Locate every blood parasite and identify its species.
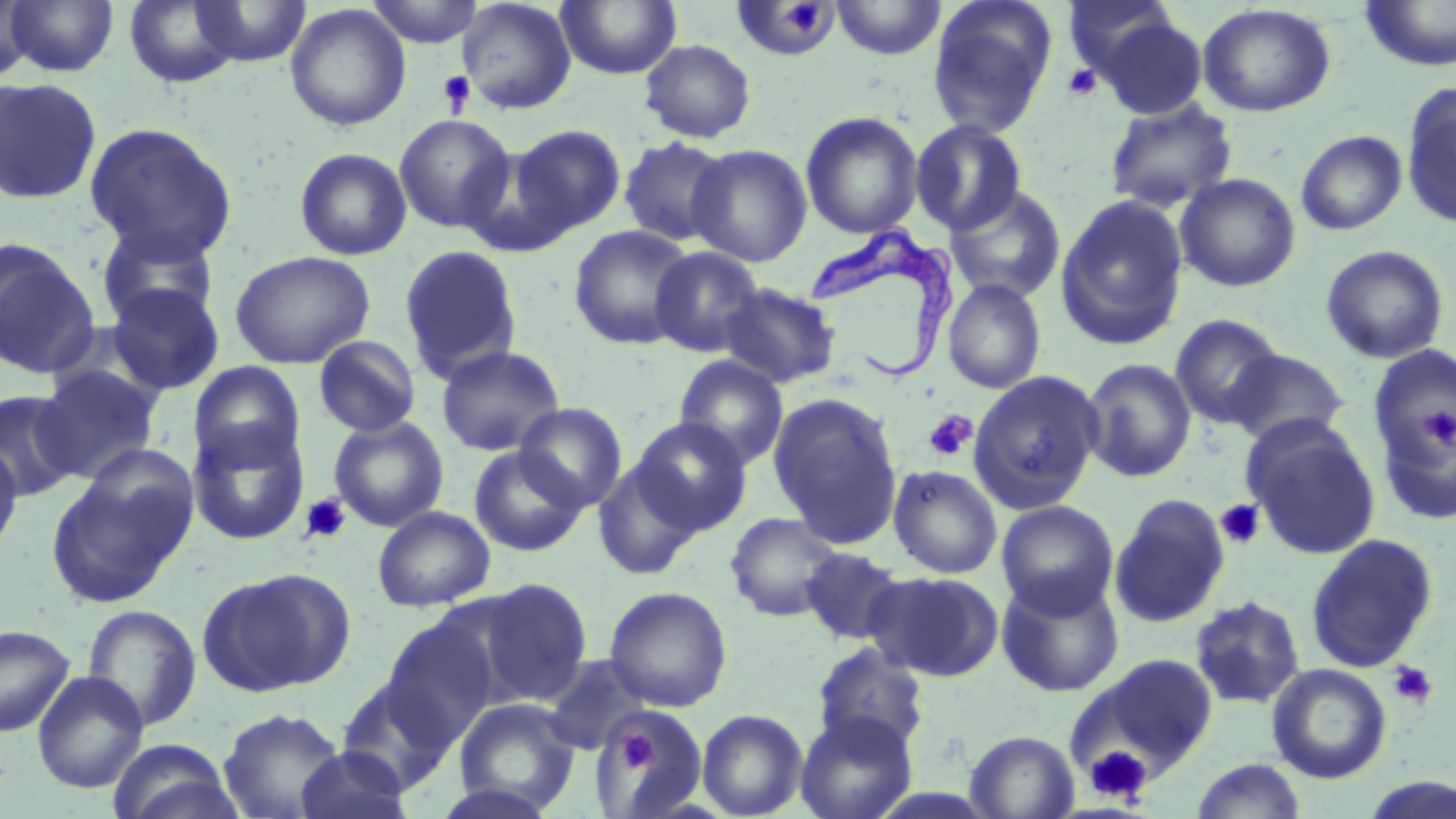

Approximate bounding boxes as [x1, y1, x2, y2] in pixels.
Trypanosoma brucei: [807, 222, 962, 383].
No Plasmodium falciparum, Plasmodium ovale, Plasmodium malariae, Plasmodium vivax, or Babesia divergens observed.

Summary:
  - Uninfected red blood cell locations: [4, 0, 119, 77], [365, 0, 485, 47], [457, 0, 577, 115], [555, 0, 682, 80], [831, 0, 945, 60], [1063, 0, 1181, 84], [1360, 0, 1456, 71], [0, 1, 38, 82], [125, 1, 243, 88], [191, 1, 312, 67], [730, 1, 842, 63], [927, 1, 1058, 138], [1198, 3, 1337, 117], [284, 4, 411, 131], [1092, 13, 1209, 120], [640, 39, 756, 143], [0, 77, 102, 204], [1401, 84, 1456, 228], [1105, 98, 1237, 213], [800, 110, 924, 239], [393, 113, 516, 234], [910, 118, 1028, 235], [84, 122, 238, 263], [507, 125, 626, 239], [1296, 130, 1407, 235], [617, 136, 733, 247], [686, 143, 812, 267], [293, 147, 413, 260], [1175, 173, 1301, 292], [945, 185, 1066, 304], [1055, 194, 1190, 350], [95, 223, 220, 331], [568, 225, 696, 350], [0, 238, 100, 378], [398, 244, 524, 385], [1320, 245, 1449, 363], [649, 246, 765, 358], [229, 250, 376, 369], [943, 279, 1046, 394], [718, 282, 842, 389], [106, 283, 224, 395], [1170, 313, 1285, 428], [313, 335, 422, 438], [435, 345, 565, 456], [1368, 346, 1456, 468], [1225, 349, 1349, 448], [674, 354, 789, 470], [1081, 358, 1196, 483], [189, 361, 306, 471], [32, 365, 162, 482], [968, 370, 1104, 513], [0, 390, 81, 503], [768, 393, 904, 547], [1375, 393, 1456, 527], [514, 402, 628, 511], [329, 416, 448, 532], [630, 417, 754, 536], [1243, 419, 1381, 560], [187, 421, 310, 545], [0, 441, 23, 558], [468, 445, 587, 557], [592, 458, 702, 580], [888, 465, 1002, 579], [45, 471, 188, 608], [1109, 493, 1230, 627], [996, 500, 1119, 617], [372, 506, 495, 612], [725, 512, 845, 622], [1305, 533, 1439, 673], [800, 546, 907, 645], [199, 567, 356, 697], [865, 570, 1003, 681], [996, 573, 1125, 697], [469, 579, 593, 707], [604, 586, 733, 712], [1188, 595, 1306, 709], [81, 604, 202, 732], [380, 616, 500, 744], [0, 624, 75, 736], [811, 641, 929, 754], [1070, 654, 1218, 784], [543, 655, 653, 755], [1267, 664, 1392, 784], [32, 671, 148, 793], [335, 676, 459, 794], [453, 698, 581, 813], [596, 705, 703, 813], [217, 707, 348, 819], [697, 709, 808, 818], [795, 712, 918, 819], [965, 730, 1079, 818], [107, 739, 242, 819], [294, 745, 414, 819], [1191, 758, 1307, 818], [1358, 774, 1456, 818], [427, 782, 562, 819]
  - Platelet locations: [782, 4, 830, 33], [1062, 63, 1102, 101], [437, 71, 475, 114], [1423, 408, 1456, 449], [924, 410, 978, 462], [300, 494, 351, 544], [1215, 499, 1266, 550], [1386, 660, 1438, 710], [615, 730, 658, 771], [1085, 745, 1152, 804]
  - Slide-level diagnosis: Trypanosoma brucei
  - Preparation: thin blood film
  - Modality: optical microscopy
  - Field of view: one of a larger specimen
  - Stain: May-Grünwald-Giemsa
  - Magnification: 1000x
  - Image size: 1456×819 pixels